Classify this cell by malaria status.
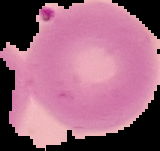

Parasitized.

Image is 160×151 pixels. From a thin blood smear. Cell region segmented out of the field of view; the surrounding area is masked to black.